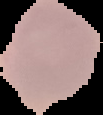

The area outside the segmented cell region is set to black. Malaria status: parasitized. Image is 103×115 pixels. From a thin blood film.